Assess the morphology of the red blood cells.
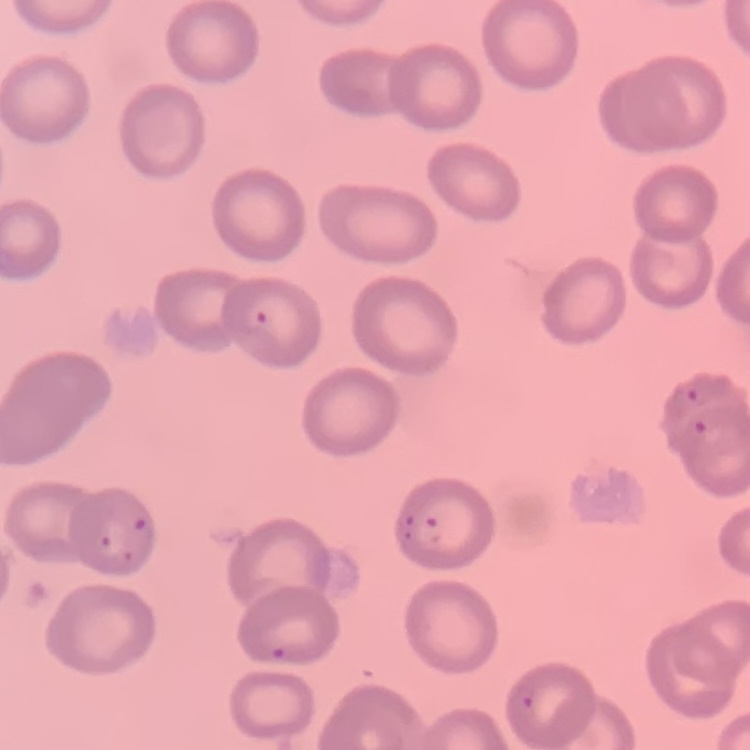
No rouleaux formation.

stain = Field's or Giemsa
image type = square crop of a larger photomicrograph
preparation = thin blood film